Give the extent of all Trypanosoma brucei.
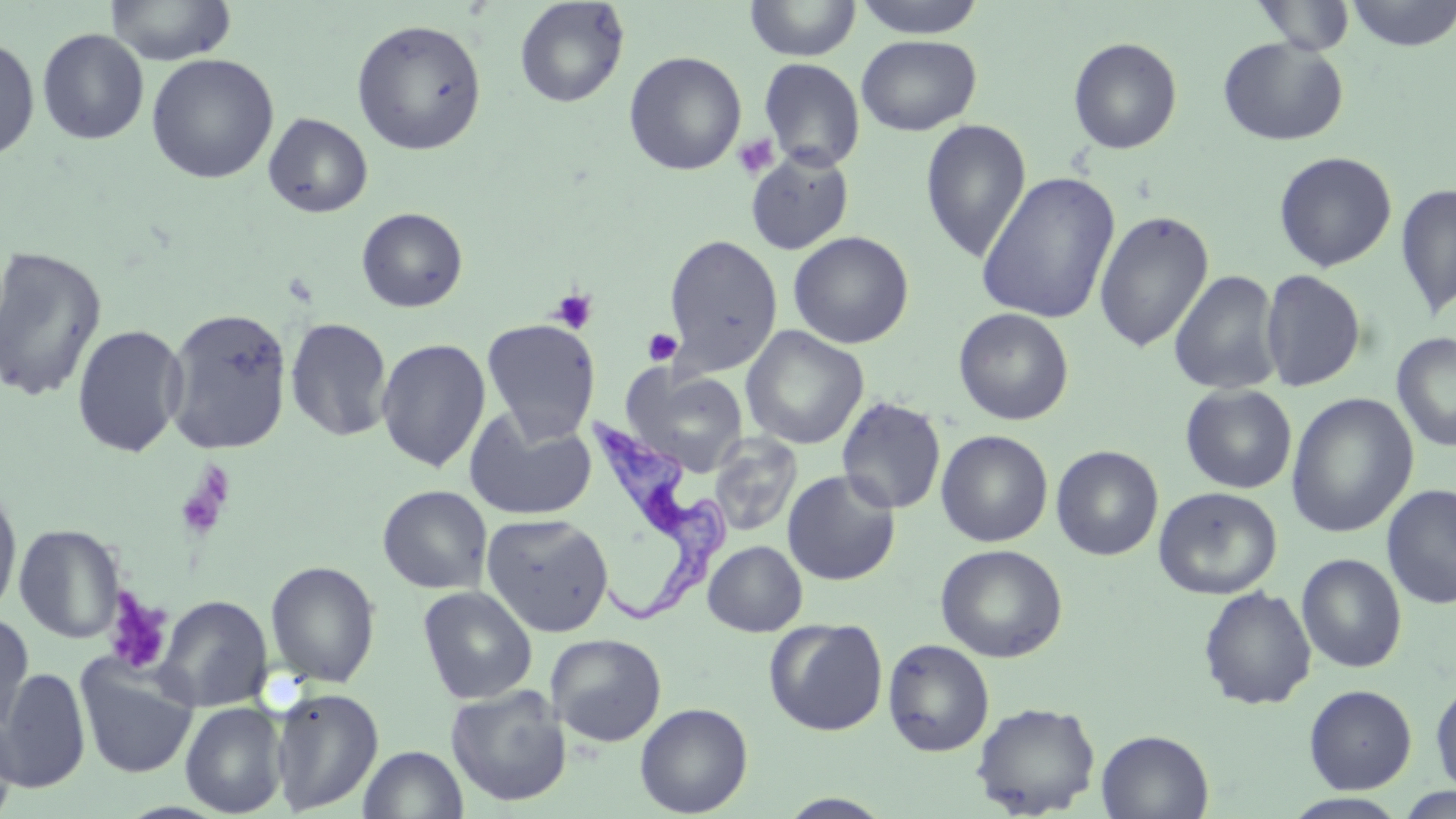
Approximate bounding boxes as (x1,y1)-(x2,y2) corner pairs in pixels.
Trypanosoma brucei: (583,411)-(731,628).

slide-level diagnosis = Trypanosoma brucei
uninfected red blood cell locations = approximate bounding boxes as (x1,y1)-(x2,y2) corner pairs in pixels: (103,0)-(238,66), (514,0)-(629,108), (744,0)-(861,61), (852,0)-(988,39), (1342,0)-(1456,50), (1253,1)-(1356,55), (351,19)-(487,155), (37,28)-(150,145), (0,35)-(40,161), (856,35)-(981,136), (1068,36)-(1183,154), (1217,36)-(1349,146), (624,51)-(747,176), (146,53)-(279,184), (757,57)-(866,172), (263,113)-(373,218), (919,119)-(1032,264), (745,150)-(854,255), (1273,151)-(1397,272), (976,171)-(1121,325), (1395,182)-(1456,320), (356,207)-(468,312), (1095,210)-(1214,352), (788,231)-(914,349), (663,234)-(783,377), (0,245)-(107,404), (1260,269)-(1367,392), (1169,270)-(1283,396), (164,307)-(293,455), (953,307)-(1074,425), (285,316)-(394,442), (481,318)-(601,442), (71,323)-(188,457), (740,326)-(869,449), (1392,333)-(1456,452), (376,338)-(491,473), (626,368)-(749,475), (1180,384)-(1298,494), (1285,393)-(1418,538), (836,396)-(946,515), (464,408)-(597,521), (936,430)-(1053,547), (707,433)-(803,537), (1050,445)-(1163,561), (782,469)-(901,586), (1381,484)-(1456,609), (377,485)-(492,594), (1153,486)-(1282,599), (0,487)-(23,618), (481,513)-(614,637), (13,523)-(127,644), (704,540)-(807,636), (935,544)-(1068,663), (1296,553)-(1407,673), (264,560)-(381,688), (418,585)-(537,704), (1198,586)-(1317,710), (151,594)-(273,712), (0,613)-(34,737), (764,618)-(888,736), (545,633)-(667,747), (882,638)-(995,757), (75,653)-(198,779), (0,668)-(91,792), (1430,679)-(1456,796), (1303,684)-(1417,794), (445,685)-(572,807), (269,687)-(384,814), (180,701)-(287,817), (971,701)-(1100,817), (635,702)-(753,817), (0,714)-(19,819), (1096,729)-(1214,818), (358,745)-(468,819), (1394,785)-(1456,817), (776,793)-(897,818), (1281,793)-(1411,818)
stain = May-Grünwald-Giemsa
image size = 1456×819 pixels
platelet locations = approximate bounding boxes as (x1,y1)-(x2,y2) corner pairs in pixels: (732,133)-(780,180), (550,288)-(599,333), (642,328)-(682,367), (173,464)-(237,543), (102,590)-(173,675)
preparation = thin blood smear
modality = optical microscopy
field of view = one of a larger specimen
magnification = 1000x